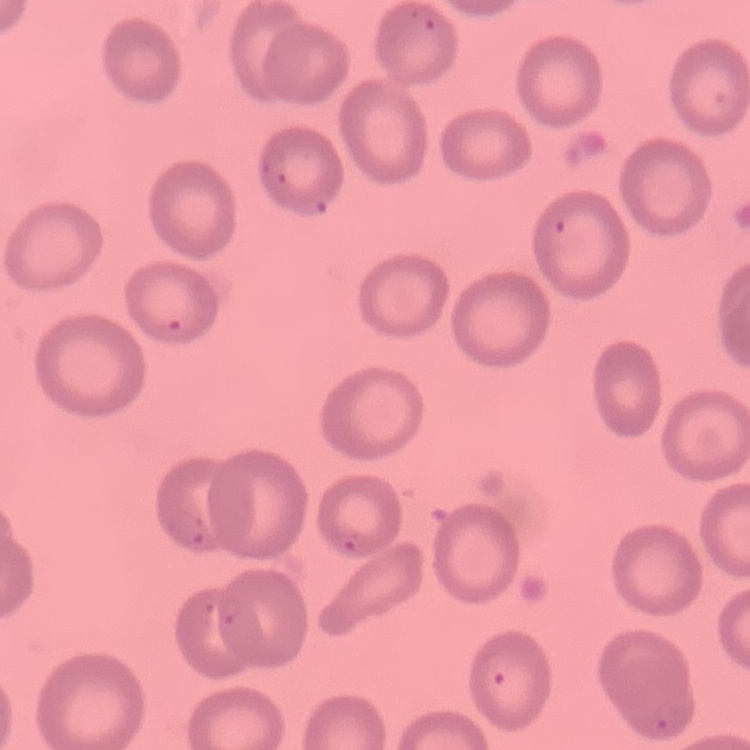
Summary:
  - Red blood cell morphology: no rouleaux formation
  - Preparation: thin blood smear
  - Image type: square crop of a larger photomicrograph
  - Stain: Field's or Giemsa